Outline each uninfected red blood cell.
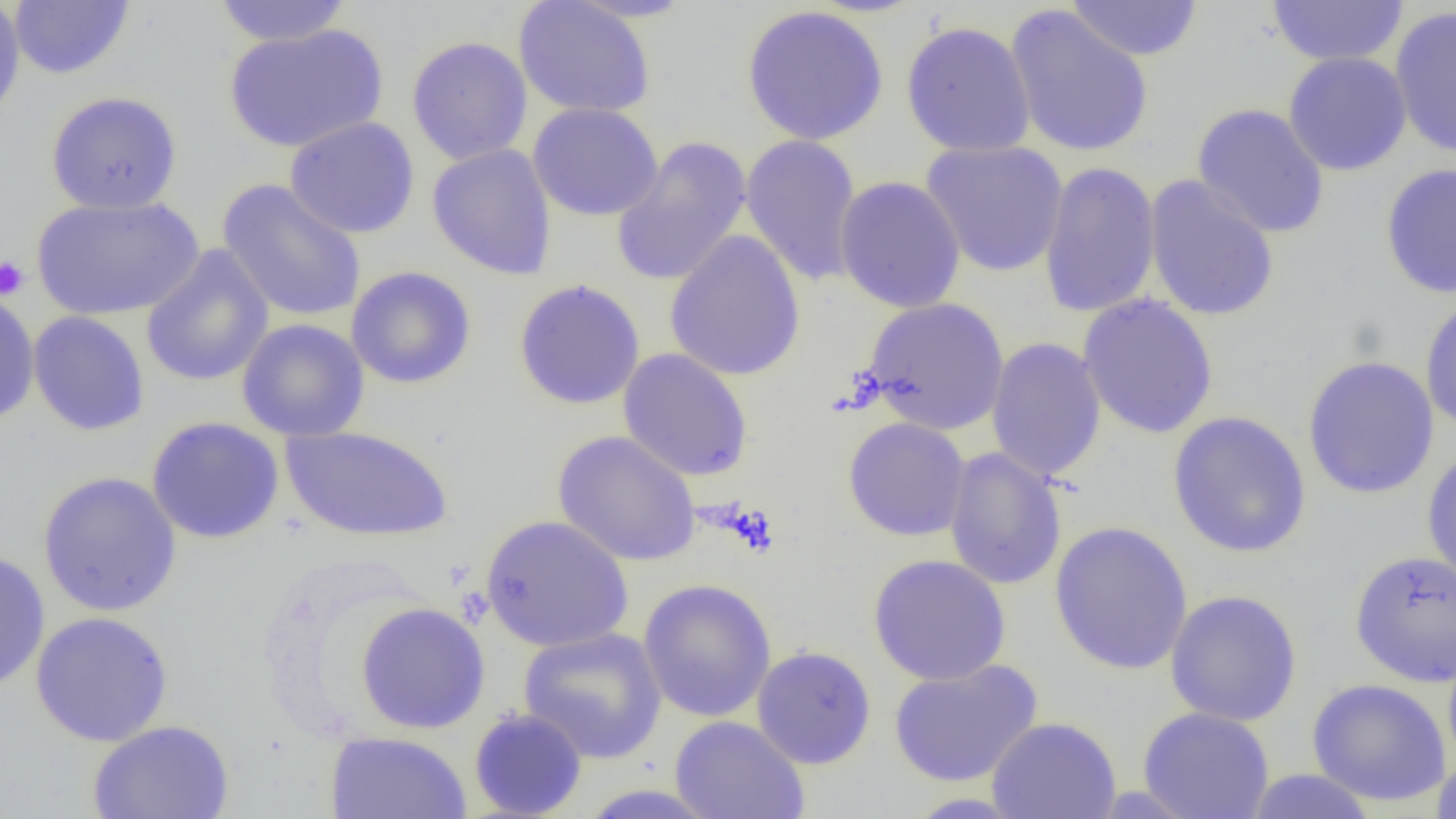

Approximate bounding boxes as [x1, y1, x2, y2] in pixels.
Uninfected red blood cells: [0, 0, 25, 124], [212, 0, 354, 46], [513, 0, 656, 118], [1066, 0, 1204, 61], [1265, 0, 1409, 67], [9, 1, 135, 80], [740, 5, 889, 146], [1005, 5, 1154, 158], [1389, 6, 1456, 159], [900, 20, 1037, 157], [223, 24, 388, 153], [406, 36, 533, 166], [1283, 52, 1412, 176], [45, 90, 183, 215], [527, 103, 663, 221], [1192, 103, 1330, 239], [285, 116, 420, 239], [740, 134, 863, 288], [611, 136, 752, 288], [920, 140, 1069, 278], [427, 143, 557, 280], [1039, 161, 1161, 318], [1380, 162, 1456, 299], [1143, 175, 1280, 322], [834, 176, 966, 314], [217, 178, 366, 323], [31, 193, 203, 321], [664, 230, 805, 382], [140, 245, 274, 388], [345, 266, 477, 389], [513, 278, 645, 410], [0, 289, 40, 428], [1078, 294, 1219, 439], [1419, 294, 1456, 431], [862, 297, 1010, 436], [28, 311, 150, 436], [236, 318, 370, 442], [986, 337, 1107, 483], [617, 348, 754, 482], [1302, 355, 1439, 500], [1168, 411, 1311, 558], [146, 416, 284, 544], [842, 417, 971, 541], [282, 425, 453, 543], [552, 430, 701, 566], [943, 447, 1067, 591], [1421, 448, 1456, 588], [37, 470, 182, 617], [479, 514, 634, 652], [1050, 520, 1193, 675], [0, 549, 50, 694], [1349, 549, 1456, 687], [867, 553, 1011, 686], [638, 577, 777, 722], [1164, 589, 1303, 727], [355, 601, 490, 734], [29, 611, 174, 747], [518, 626, 667, 764], [1442, 642, 1456, 776], [751, 645, 877, 769], [888, 659, 1043, 787], [1307, 677, 1451, 807], [1138, 706, 1275, 818], [468, 708, 588, 818], [669, 715, 810, 819], [986, 716, 1121, 819], [86, 719, 235, 819], [325, 730, 472, 818], [1431, 755, 1456, 819], [1242, 769, 1380, 818].

slide_level_diagnosis: no evidence of blood parasites
platelet_locations: 'approximate bounding boxes as [x1, y1, x2, y2] in pixels: [0, 256, 31, 301]'
modality: optical microscopy
field_of_view: one of a larger specimen
preparation: thin blood film
image_size: 1456×819 pixels
magnification: 1000x